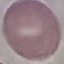 Result: no malaria parasites seen. Cell patch, automatically extracted from a larger field of view and resized to 64 × 64 pixels. Thin blood smear. Acquired by smartphone through the microscope eyepiece. Giemsa-stained preparation.